Classify this cell by malaria status.
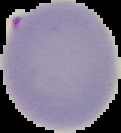
Uninfected.

Summary:
  - Preparation: thin blood film
  - Image size: 121×133 pixels
  - Image type: segmented cell region on a black background